Assess the morphology of the erythrocytes.
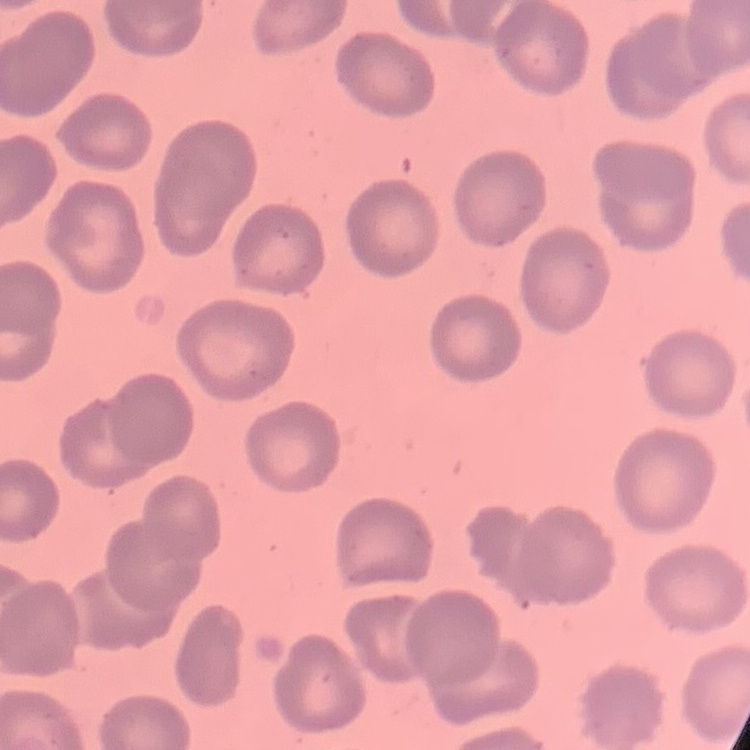

They show no rouleaux formation.

Stained with either Field's or Giemsa. One tile cut from a larger photomicrograph. Thin blood smear.